Identify the blood parasite species.
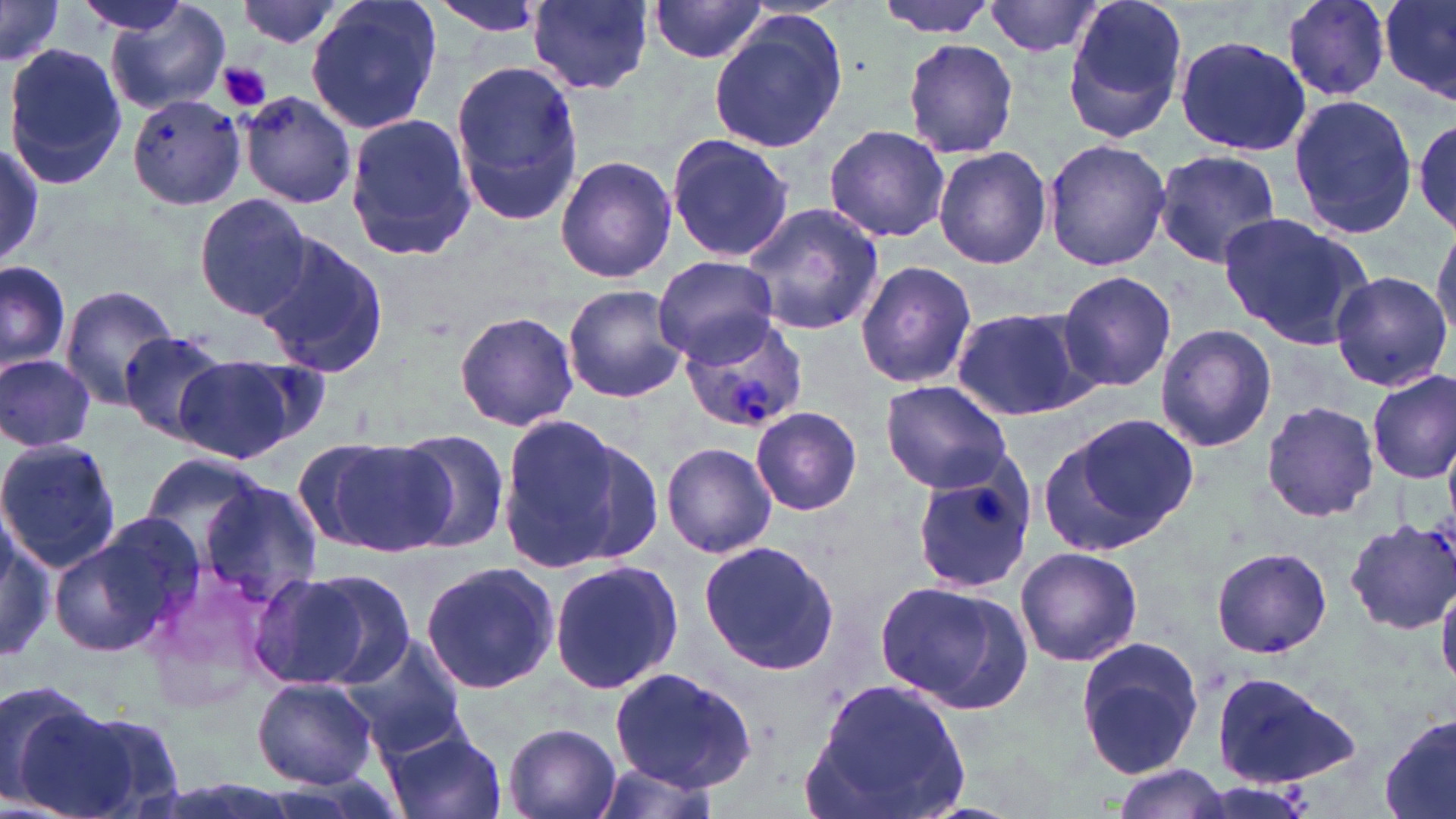

Plasmodium ovale.

Summary:
  - Coordinate format: approximate bounding boxes as (x1, y1, x2, y2) in pixels
  - Uninfected red blood cell locations: (71, 0, 197, 36), (303, 0, 443, 137), (428, 0, 549, 40), (527, 0, 656, 94), (651, 0, 766, 64), (873, 0, 1000, 37), (984, 0, 1104, 59), (1061, 0, 1192, 142), (1280, 0, 1393, 100), (1377, 0, 1456, 103), (233, 1, 346, 49), (0, 2, 64, 69), (103, 3, 231, 113), (706, 12, 846, 155), (1174, 35, 1312, 158), (902, 39, 1019, 159), (4, 44, 125, 185), (450, 60, 585, 226), (238, 91, 356, 209), (127, 94, 246, 210), (1287, 95, 1418, 239), (1412, 112, 1455, 237), (344, 114, 478, 260), (823, 123, 951, 244), (666, 134, 796, 263), (1041, 137, 1172, 271), (0, 142, 46, 267), (931, 145, 1053, 270), (1153, 150, 1282, 270), (554, 154, 677, 284), (192, 194, 315, 321), (738, 201, 884, 335), (1218, 212, 1375, 351), (1432, 226, 1456, 343), (254, 235, 388, 378), (653, 256, 780, 364), (0, 260, 70, 376), (855, 261, 978, 390), (1055, 269, 1177, 393), (1331, 269, 1452, 392), (561, 284, 687, 402), (59, 285, 184, 411), (950, 303, 1100, 422), (453, 312, 580, 431), (1154, 322, 1277, 453), (117, 327, 232, 443), (1, 352, 96, 452), (173, 356, 299, 464), (230, 357, 334, 449), (1368, 368, 1455, 485), (879, 380, 1015, 493), (1260, 400, 1381, 522), (749, 406, 866, 516), (1049, 413, 1199, 548), (497, 414, 656, 573), (389, 428, 513, 553), (301, 434, 453, 557), (0, 435, 121, 576), (661, 440, 777, 559), (909, 462, 1036, 597), (197, 475, 325, 608), (1, 515, 53, 664), (1341, 519, 1456, 637), (49, 526, 181, 656), (698, 540, 841, 676), (1015, 545, 1142, 667), (1210, 547, 1333, 659), (548, 560, 684, 696), (421, 561, 559, 693), (256, 565, 416, 693), (874, 578, 1033, 716), (1437, 581, 1456, 688), (336, 631, 472, 756), (1074, 636, 1205, 778), (609, 665, 757, 793), (1209, 670, 1366, 788), (800, 674, 973, 819), (252, 677, 378, 787), (0, 684, 123, 818), (49, 707, 191, 819), (1380, 712, 1456, 819), (502, 723, 624, 819), (384, 727, 508, 819), (585, 759, 730, 819), (1111, 765, 1237, 819)
  - Plasmodium ovale-infected red blood cell locations: (679, 311, 810, 430)
  - Platelet locations: (219, 62, 271, 112)
  - Stain: May-Grünwald-Giemsa
  - Modality: optical microscopy
  - Magnification: 1000x
  - Preparation: thin blood smear
  - Field of view: single
  - Image size: 1456×819 pixels